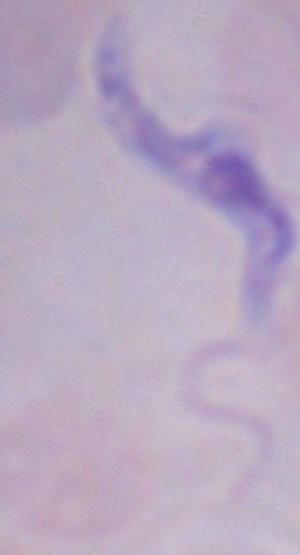
A trypanosome is seen. Photomicrograph. Captured at 1000x magnification.